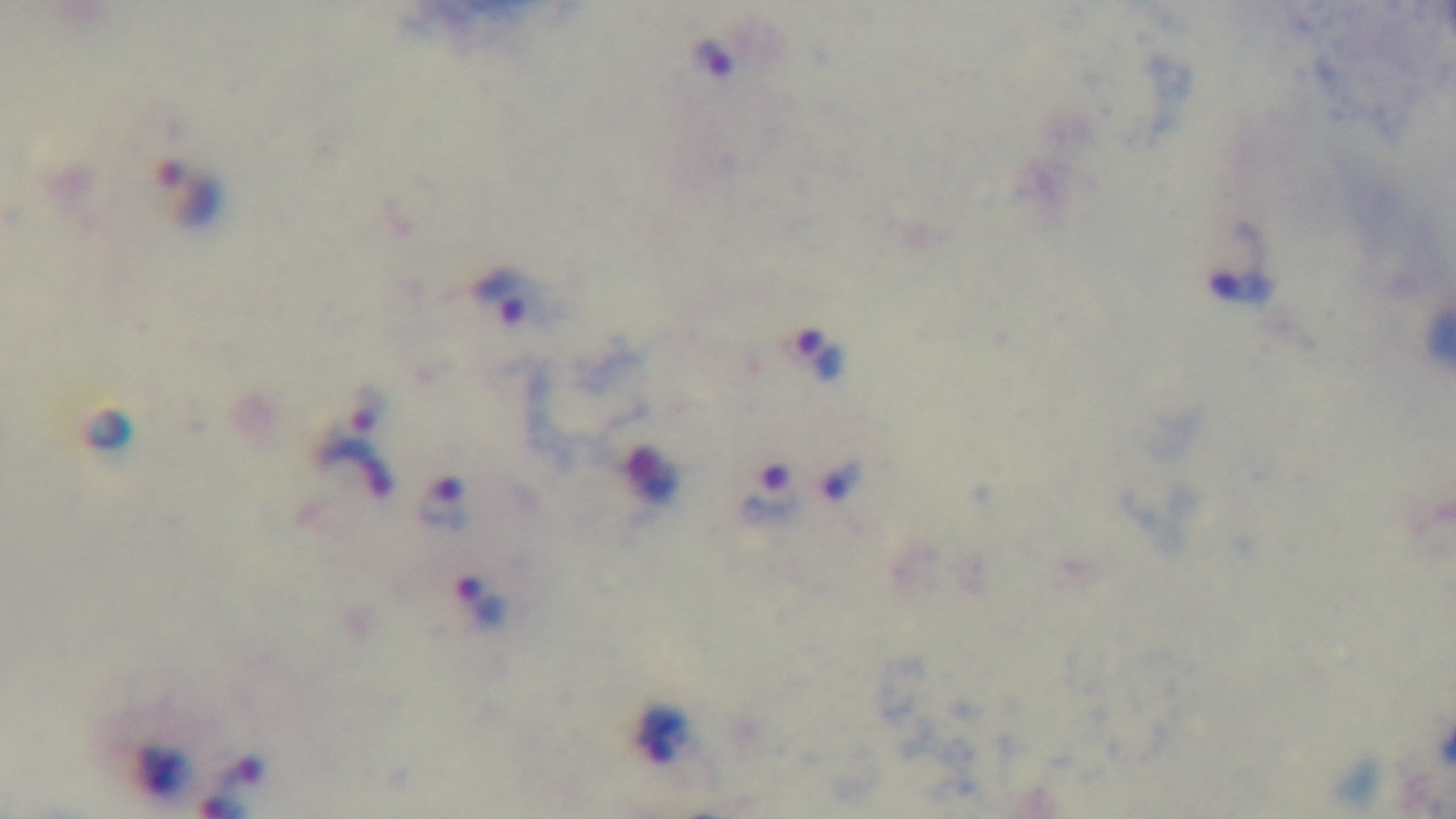

Malaria status: infected. Preparation: thick. Light microscopy. One field from the slide. 100x oil-immersion objective. Captured with a mounted 4K digital camera. Giemsa-stained.